Assess the morphology of the red blood cells.
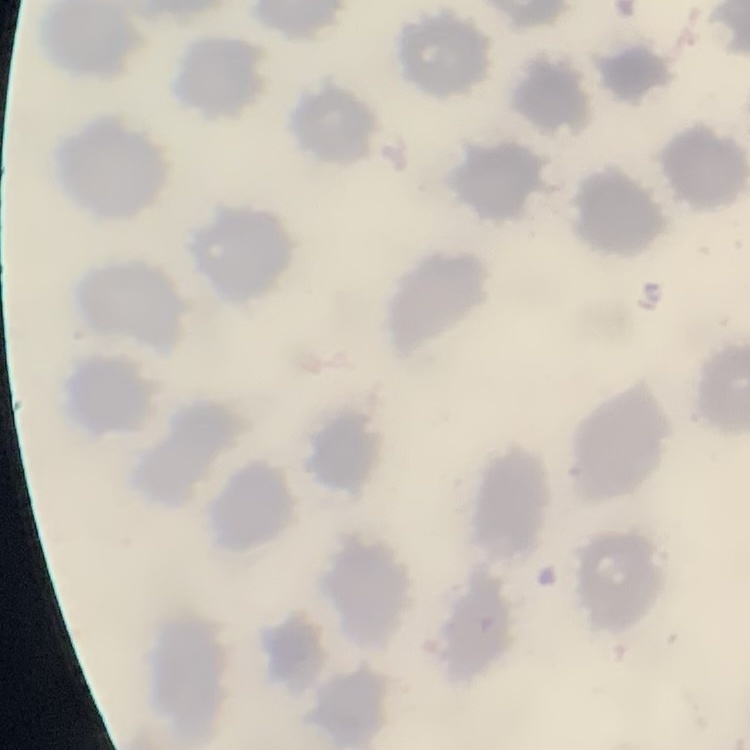
They show no rouleaux formation.

One tile cut from a larger photomicrograph. Field's or Giemsa stain. Thin peripheral smear.